Assess this cell for malaria.
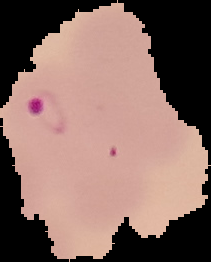
It is parasitized.

Summary:
  - Image type: segmented cell region on a black background
  - Image size: 211×262 pixels
  - Preparation: thin blood smear